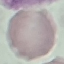
Summary:
  - Result: no malaria parasites seen
  - Capture: smartphone camera at the microscope eyepiece
  - Image type: cell patch, automatically extracted from a larger field of view and resized to 64 × 64 pixels
  - Stain: Giemsa
  - Preparation: thin smear